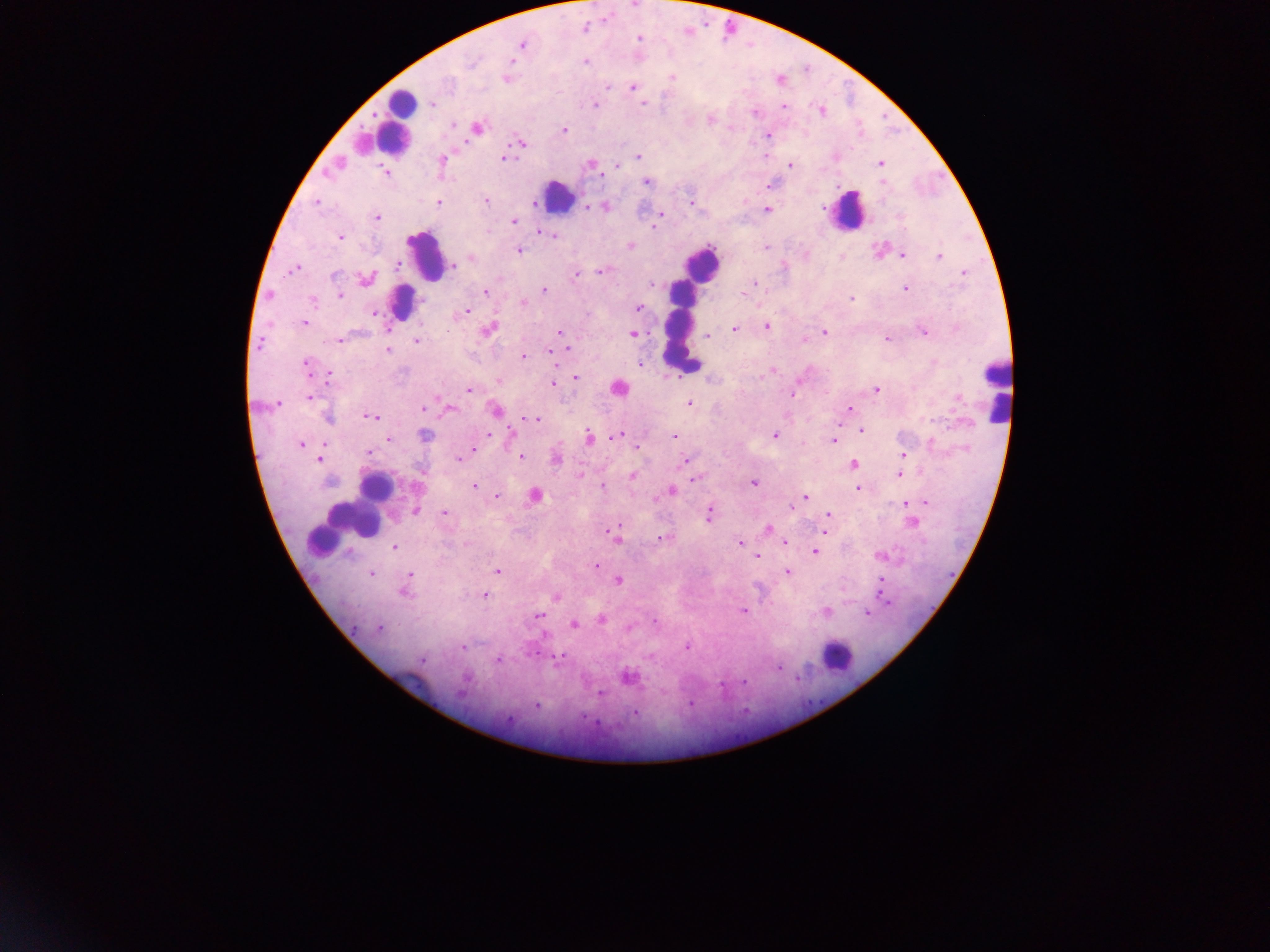
Approximate centers as x y in pixels. Leukocyte locations: 402 105; 396 123; 556 197; 846 211; 425 256; 702 263; 401 301; 680 321; 617 387; 995 389; 373 486; 368 498; 349 523; 836 657. Malaria parasite locations: 583 27; 639 38; 521 45; 584 61; 506 77; 671 77; 607 87; 632 88; 431 104; 595 104; 643 104; 782 106; 821 110; 755 112; 710 119; 452 124; 475 128; 564 129; 767 135; 520 142; 765 154; 638 156; 504 158; 442 160; 880 163; 337 164; 591 164; 790 164; 617 166; 383 170; 646 181; 486 201; 535 201; 316 202; 691 202; 438 203; 585 206; 603 206; 766 209; 661 213; 376 217; 513 221; 657 221; 655 227; 541 232; 552 234; 340 237; 630 245; 766 247; 518 250; 878 251; 804 255; 902 255; 840 256; 940 256; 471 257; 398 264; 451 264; 295 268; 602 271; 575 273; 964 274; 365 279; 754 283; 651 284; 904 288; 544 290; 485 291; 268 294; 339 294; 743 296; 850 297; 313 300; 522 303; 638 308; 373 312; 464 312; 305 323; 766 327; 733 328; 488 329; 923 330; 561 332; 824 332; 632 334; 707 335; 887 338; 339 340; 804 340; 417 341; 260 344; 566 345; 387 351; 550 351; 523 357; 639 364; 306 367; 773 369; 328 377; 574 377; 498 381; 552 384; 876 389; 468 390; 792 392; 308 396; 277 403; 689 404; 425 406; 447 409; 849 409; 495 410; 327 416; 372 416; 533 419; 861 430; 488 433; 509 434; 618 435; 774 435; 424 436; 674 436; 387 438; 588 438; 833 440; 301 444; 637 447; 473 448; 369 452; 903 455; 519 457; 556 457; 459 458; 319 459; 684 461; 852 464; 580 474; 900 474; 631 476; 695 478; 753 482; 472 486; 416 487; 602 487; 857 487; 670 491; 536 495; 496 496; 805 496; 925 502; 905 503; 788 507; 415 510; 444 513; 709 513; 827 513; 912 522; 613 529; 766 529; 824 532; 614 537; 661 539; 740 543; 784 543; 394 547; 814 551; 880 555; 757 557; 595 564; 497 570; 787 572; 370 573; 408 575; 618 580; 880 582; 403 590; 484 595; 556 596; 744 611; 826 612; 867 613; 537 615; 602 620; 655 621; 575 624; 379 627; 629 628; 462 646; 686 646; 555 657; 421 660; 497 660; 779 666; 627 676; 599 694; 692 703; 536 706; 635 712. Sample from Ghana. Image is 1270×952 pixels. One field of view. Thick blood film. Mobile-phone photograph taken through the microscope.